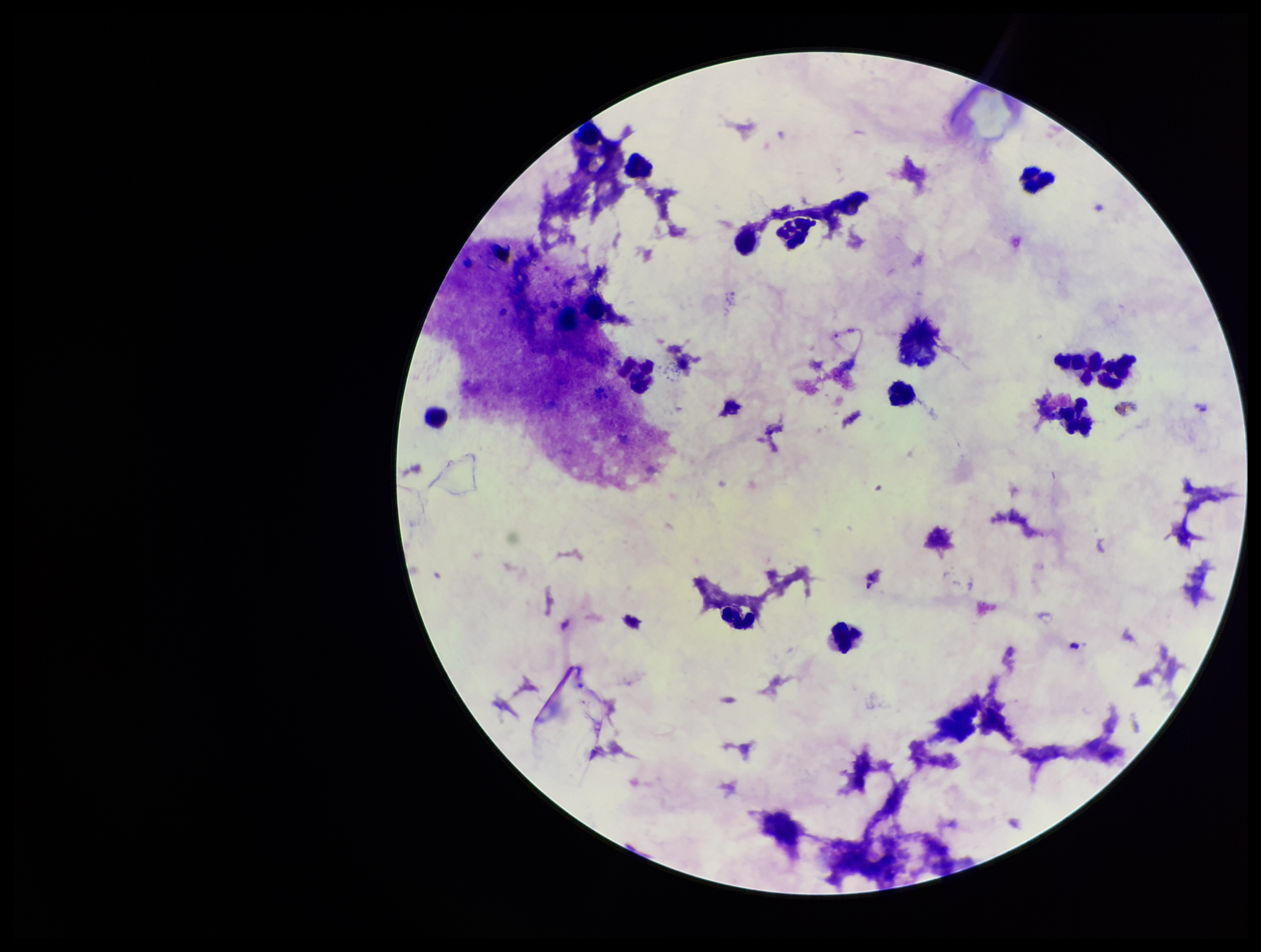
image size = 1261×952 pixels
patient malaria status = negative
stain = Giemsa
preparation = thick smear
leukocyte count = 15
parasite count = 0
field of view = single
Plasmodium parasites = none seen
capture = smartphone photograph through the microscope eyepiece